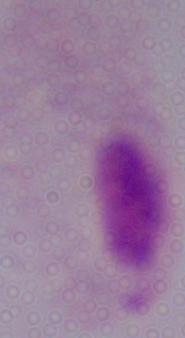

identification = trichomonad
modality = photomicrograph
magnification = 1000x